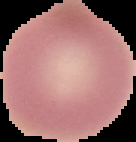

malaria status = uninfected
image size = 136×142 pixels
image type = segmented cell region with the area outside set to black
preparation = thin blood film